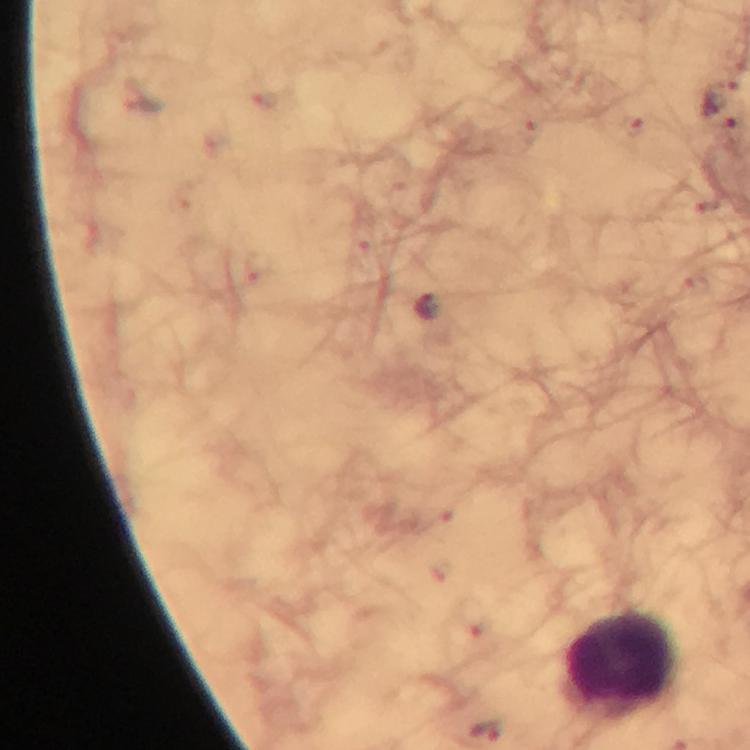

cropped_from: a single field of view
leukocyte_locations: 'approximate object centers, in pixels from the top-left corner: (x=620, y=662)'
immersion_oil: used
malaria_parasite_locations: 'approximate object centers, in pixels from the top-left corner: (x=428, y=307)'
magnification: 100x
capture: smartphone mounted on the microscope
context: from a malaria diagnostic workup
preparation: thick blood film
stain: Giemsa
image_size: 750×750 pixels